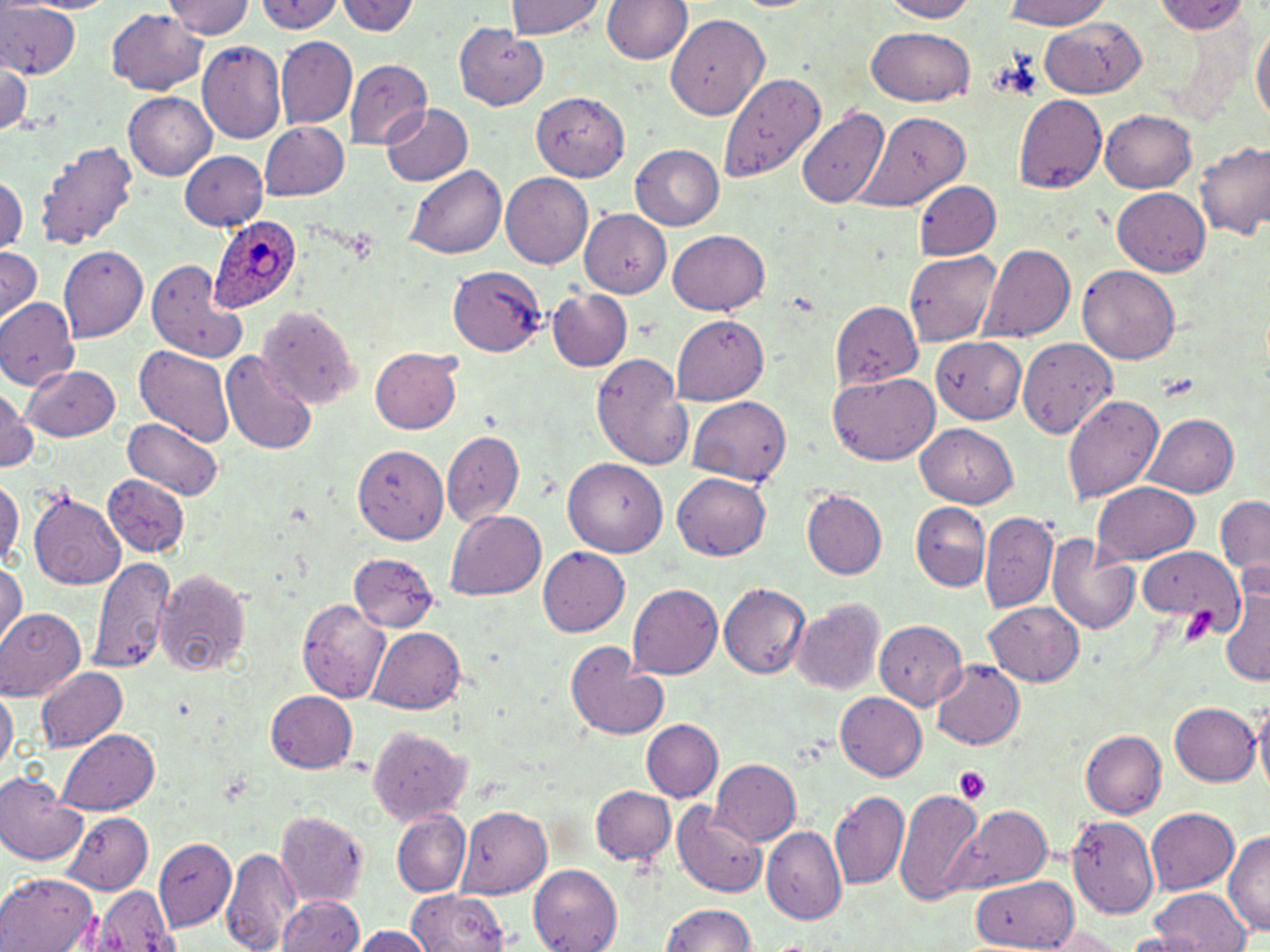

Approximate bounding boxes as (x1, y1, x2, y2) in pixels. Uninfected red blood cell locations: (21, 0, 120, 15), (167, 0, 255, 39), (341, 0, 417, 38), (506, 0, 607, 39), (603, 0, 691, 66), (879, 0, 981, 22), (998, 0, 1119, 30), (257, 1, 347, 34), (1154, 1, 1251, 35), (0, 2, 81, 79), (103, 9, 211, 93), (666, 13, 770, 118), (1042, 15, 1148, 98), (1252, 19, 1269, 136), (454, 22, 548, 109), (866, 27, 976, 107), (276, 36, 356, 129), (197, 41, 287, 144), (343, 60, 431, 147), (1, 61, 33, 137), (355, 74, 457, 174), (718, 77, 823, 185), (123, 92, 216, 180), (531, 92, 629, 181), (1013, 95, 1107, 193), (797, 102, 891, 209), (380, 105, 472, 187), (1101, 109, 1198, 192), (859, 110, 970, 213), (260, 122, 351, 200), (39, 138, 138, 251), (1193, 141, 1270, 239), (631, 144, 724, 230), (179, 150, 267, 231), (406, 163, 507, 258), (500, 171, 593, 266), (0, 173, 24, 253), (913, 180, 1000, 261), (1115, 188, 1212, 274), (580, 210, 674, 297), (670, 227, 769, 315), (981, 242, 1075, 344), (58, 245, 147, 343), (0, 247, 42, 327), (904, 250, 1003, 345), (148, 257, 249, 363), (450, 264, 546, 355), (1077, 266, 1181, 363), (547, 287, 633, 372), (0, 299, 79, 391), (832, 301, 922, 389), (257, 304, 361, 408), (671, 316, 770, 404), (932, 337, 1027, 425), (1019, 339, 1121, 438), (135, 345, 233, 445), (370, 348, 462, 435), (220, 350, 319, 454), (592, 351, 692, 469), (24, 363, 120, 441), (828, 372, 941, 465), (0, 386, 37, 475), (1062, 394, 1164, 504), (687, 396, 791, 488), (1146, 413, 1239, 499), (121, 418, 226, 502), (917, 422, 1020, 507), (442, 431, 523, 528), (355, 446, 449, 546), (564, 456, 667, 555), (0, 471, 22, 573), (673, 473, 771, 562), (104, 474, 190, 557), (1091, 482, 1201, 563), (27, 491, 126, 589), (803, 491, 886, 579), (1213, 496, 1269, 577), (911, 504, 990, 592), (448, 509, 547, 599), (980, 512, 1057, 615), (1047, 536, 1141, 634), (1136, 544, 1241, 622), (537, 546, 630, 637), (348, 550, 437, 631), (86, 556, 175, 675), (0, 562, 24, 651), (154, 568, 253, 676), (1222, 570, 1270, 692), (628, 583, 721, 682), (721, 583, 810, 680), (298, 599, 388, 704), (792, 600, 884, 696), (985, 601, 1083, 687), (0, 610, 85, 703), (875, 620, 968, 710), (365, 627, 467, 712), (565, 642, 669, 741), (929, 660, 1025, 751), (37, 667, 129, 751), (0, 685, 17, 774), (264, 690, 357, 773), (836, 693, 928, 780), (1255, 701, 1269, 801), (1169, 702, 1259, 787), (642, 719, 723, 803), (366, 725, 470, 824), (56, 730, 161, 815), (1080, 731, 1165, 818), (711, 759, 802, 847), (0, 773, 88, 865), (590, 785, 675, 866), (894, 788, 987, 904), (829, 791, 908, 889), (671, 801, 768, 899), (946, 803, 1053, 894), (457, 806, 552, 898), (1146, 807, 1240, 894), (273, 810, 369, 904), (60, 811, 153, 892), (393, 811, 470, 896), (1068, 814, 1158, 918), (763, 826, 846, 922), (1226, 830, 1270, 943), (157, 839, 238, 930), (223, 844, 302, 952), (529, 866, 622, 952), (0, 870, 99, 952), (972, 874, 1078, 949), (89, 885, 181, 952), (402, 886, 516, 952), (1147, 889, 1247, 952), (278, 895, 363, 952), (658, 903, 760, 952), (1050, 922, 1126, 952), (352, 925, 433, 952). Plasmodium ovale-infected red blood cell locations: (210, 208, 308, 313). Platelet locations: (341, 228, 380, 261), (1154, 374, 1200, 398), (1184, 604, 1219, 644), (954, 766, 992, 805). Slide-level diagnosis: Plasmodium ovale. Thin blood film. Image is 1270×952 pixels. One field of a larger specimen. 1000x magnification. Optical microscopy. May-Grünwald-Giemsa-stained preparation.